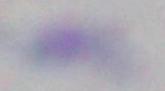

Summary:
  - Modality: micrograph
  - Identification: Toxoplasma gondii
  - Magnification: 1000x